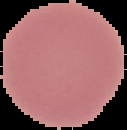
From a thin blood smear. Cell region segmented out of the field of view; the surrounding area is masked to black. Image is 127×130 pixels. Result: no malaria parasites seen.